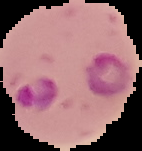
image type = segmented cell region on a black background
preparation = thin blood smear
result = Plasmodium parasites detected
image size = 142×151 pixels